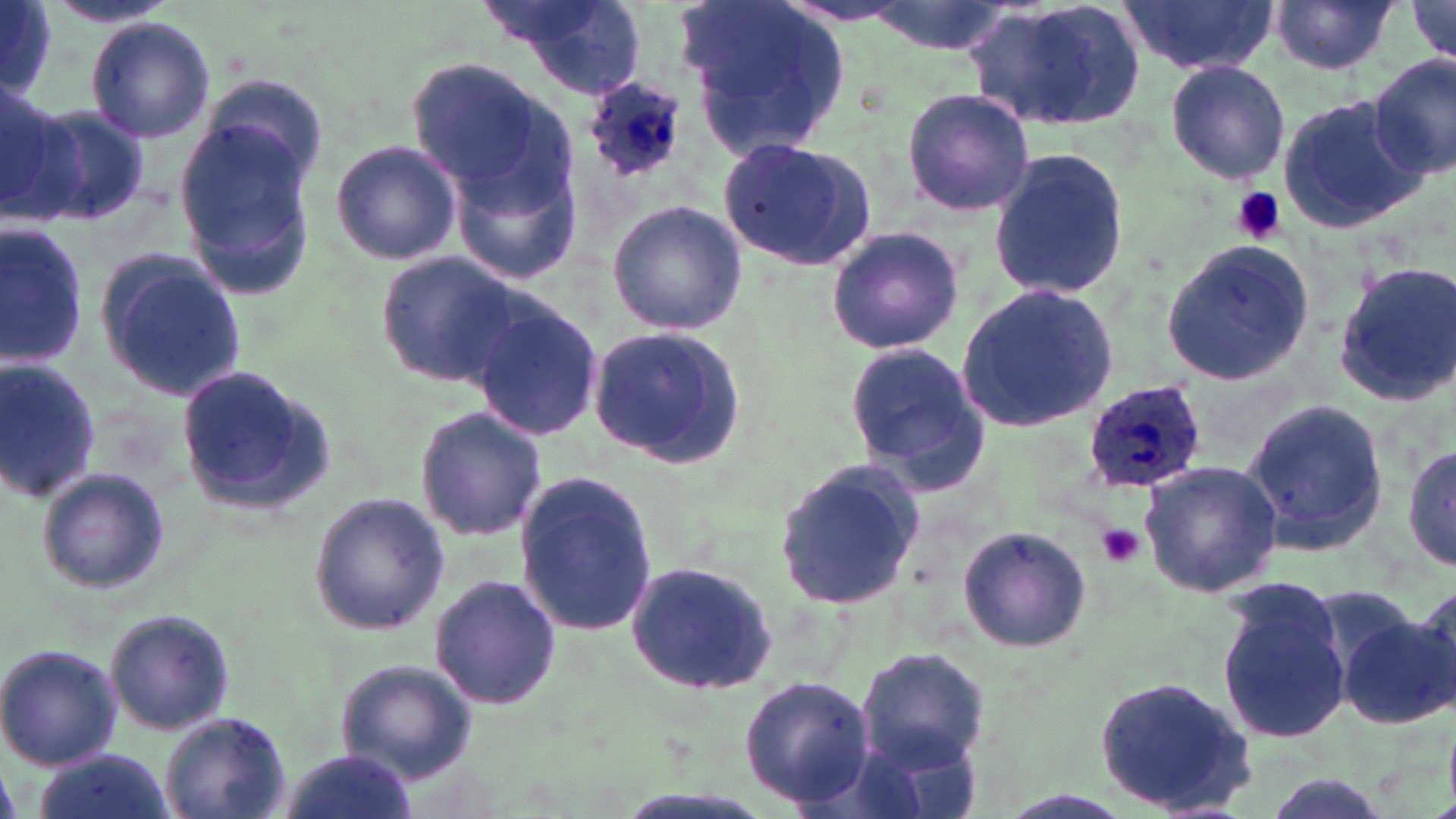

slide-level diagnosis = Plasmodium ovale
stain = May-Grünwald-Giemsa
Plasmodium ovale-infected red blood cell locations = approximate bounding boxes as [x1, y1, x2, y2] in pixels: [583, 75, 693, 186], [1082, 380, 1210, 494]
uninfected red blood cell locations = approximate bounding boxes as [x1, y1, x2, y2] in pixels: [483, 0, 647, 100], [676, 0, 854, 158], [856, 0, 1020, 57], [966, 0, 1148, 133], [1118, 0, 1277, 74], [1269, 1, 1399, 77], [1404, 1, 1456, 71], [0, 2, 58, 97], [44, 2, 179, 31], [86, 17, 215, 141], [1371, 55, 1455, 179], [1165, 59, 1289, 186], [411, 60, 558, 194], [191, 73, 331, 203], [0, 84, 76, 227], [899, 88, 1034, 216], [1277, 92, 1424, 233], [27, 101, 152, 228], [178, 119, 319, 293], [716, 134, 879, 270], [446, 138, 586, 293], [330, 139, 461, 266], [985, 147, 1131, 303], [607, 199, 747, 337], [0, 225, 91, 368], [825, 226, 967, 355], [1156, 240, 1318, 387], [95, 252, 248, 403], [376, 252, 526, 390], [1330, 259, 1456, 406], [954, 286, 1119, 432], [469, 294, 604, 447], [586, 325, 746, 470], [843, 342, 989, 488], [0, 357, 103, 505], [173, 364, 335, 518], [1242, 397, 1388, 553], [415, 407, 547, 541], [1401, 440, 1455, 575], [1138, 460, 1283, 597], [774, 461, 924, 613], [34, 467, 170, 595], [516, 473, 658, 638], [308, 495, 450, 634], [956, 526, 1093, 653], [622, 557, 780, 694], [429, 574, 561, 712], [1216, 583, 1351, 747], [1406, 583, 1456, 713], [1306, 584, 1433, 702], [105, 608, 235, 738], [1338, 608, 1454, 728], [0, 644, 123, 770], [854, 646, 990, 770], [339, 659, 482, 784], [738, 675, 877, 810], [1093, 678, 1260, 817], [159, 712, 290, 819], [31, 750, 174, 819], [281, 750, 415, 819], [1254, 774, 1397, 819], [982, 789, 1146, 819]
magnification = 1000x
field of view = one of a larger specimen
preparation = thin blood film
modality = light microscopy
image size = 1456×819 pixels
platelet locations = approximate bounding boxes as [x1, y1, x2, y2] in pixels: [1231, 188, 1285, 243], [1098, 524, 1144, 567]